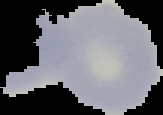
Summary:
  - Result: no Plasmodium parasites detected
  - Preparation: thin blood film
  - Image size: 163×115 pixels
  - Image type: cell region segmented out of the field of view; surrounding area masked to black